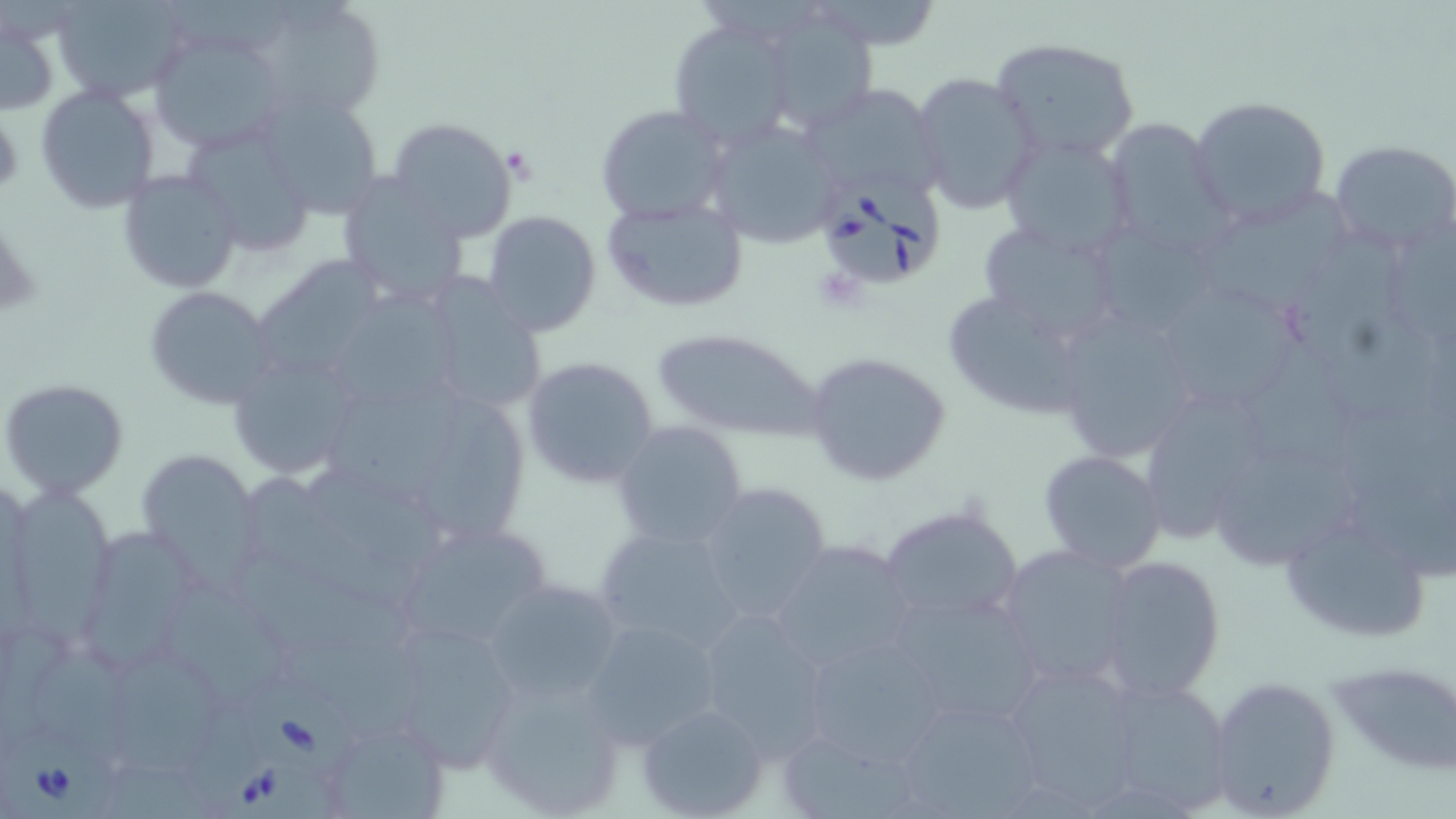
Approximate bounding boxes as (x1, y1, x2, y2) in pixels. Babesia divergens-infected red blood cell locations: (811, 175, 947, 291), (249, 680, 367, 787), (198, 699, 342, 819), (4, 729, 124, 819). Uninfected red blood cell locations: (53, 0, 193, 102), (250, 0, 389, 120), (810, 3, 947, 49), (760, 7, 881, 134), (2, 18, 59, 117), (667, 19, 796, 153), (151, 30, 288, 153), (990, 35, 1141, 163), (909, 72, 1043, 216), (33, 82, 162, 215), (799, 83, 948, 202), (253, 91, 386, 222), (1189, 94, 1331, 229), (594, 104, 730, 225), (1103, 115, 1233, 256), (705, 117, 845, 249), (387, 118, 519, 241), (999, 133, 1138, 260), (1329, 138, 1456, 254), (115, 169, 242, 293), (336, 175, 473, 305), (1187, 187, 1353, 314), (600, 196, 750, 313), (481, 211, 601, 337), (974, 219, 1130, 350), (1292, 231, 1410, 365), (259, 254, 383, 373), (439, 271, 544, 408), (1153, 283, 1302, 413), (144, 287, 275, 408), (942, 287, 1093, 420), (340, 290, 469, 410), (1053, 305, 1205, 461), (651, 327, 825, 445), (1247, 328, 1356, 467), (804, 350, 953, 488), (521, 355, 661, 489), (232, 363, 352, 477), (324, 365, 462, 494), (2, 378, 130, 500), (1134, 385, 1278, 541), (428, 394, 529, 543), (611, 419, 750, 550), (1216, 443, 1360, 571), (1038, 449, 1168, 571), (141, 451, 265, 596), (250, 474, 427, 605), (16, 481, 119, 651), (694, 481, 834, 620), (879, 502, 1025, 627), (1277, 511, 1435, 643), (397, 521, 551, 648), (592, 525, 744, 653), (84, 526, 201, 672), (767, 538, 918, 674), (995, 544, 1141, 691), (1091, 553, 1227, 705), (237, 559, 431, 732), (479, 576, 625, 704), (176, 583, 282, 714), (882, 590, 1047, 729), (692, 609, 835, 759), (578, 616, 724, 749), (382, 622, 527, 772), (800, 633, 950, 765), (29, 636, 143, 766), (994, 655, 1146, 811), (1330, 657, 1456, 776), (116, 659, 223, 774), (479, 673, 627, 818), (1204, 673, 1343, 818), (1095, 678, 1236, 815), (889, 693, 1047, 819), (637, 703, 770, 818), (328, 718, 448, 813), (781, 734, 924, 819). Slide-level diagnosis: Babesia divergens. Single field of view. Thin blood film. Image is 1456×819 pixels. May-Grünwald-Giemsa-stained preparation. Captured at 1000x magnification. Optical microscopy.